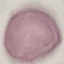

Summary:
  - Malaria status: uninfected
  - Preparation: thin blood film
  - Image type: cell patch, automatically extracted from a larger field of view and resized to 64 × 64 pixels
  - Capture: smartphone camera at the microscope eyepiece
  - Stain: Giemsa